Locate platelets.
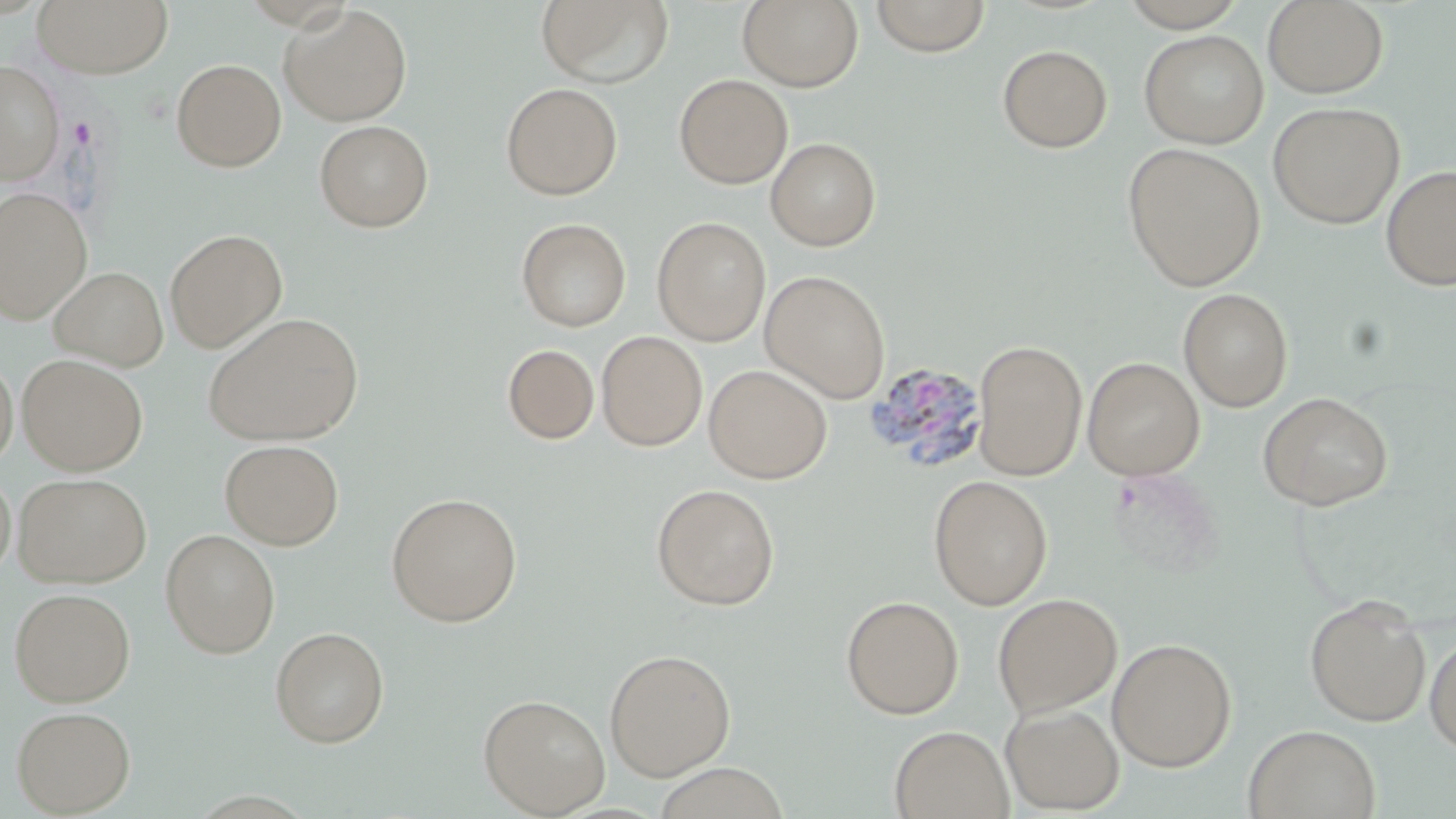
Approximate bounding boxes as (x1, y1, x2, y2) in pixels.
Platelets: (69, 118, 96, 147).

slide-level diagnosis = Plasmodium vivax
magnification = 1000x
image size = 1456×819 pixels
uninfected red blood cell locations = approximate bounding boxes as (x1, y1, x2, y2) in pixels: (33, 0, 174, 79), (535, 0, 674, 87), (738, 0, 864, 91), (869, 0, 991, 57), (1118, 0, 1249, 31), (1263, 0, 1389, 98), (279, 5, 412, 126), (1139, 29, 1268, 149), (997, 44, 1112, 153), (171, 58, 286, 172), (0, 61, 65, 184), (674, 73, 793, 189), (501, 82, 623, 200), (1267, 101, 1405, 229), (314, 120, 434, 232), (765, 136, 881, 251), (1122, 143, 1267, 290), (1381, 164, 1456, 291), (1, 187, 92, 322), (652, 216, 770, 345), (516, 217, 631, 331), (165, 229, 288, 352), (48, 265, 168, 371), (760, 269, 890, 402), (1178, 287, 1293, 412), (202, 312, 364, 446), (597, 331, 707, 451), (973, 340, 1087, 481), (502, 343, 599, 445), (19, 354, 148, 474), (0, 355, 17, 471), (1083, 357, 1204, 480), (703, 364, 832, 483), (1257, 391, 1393, 510), (219, 439, 345, 549), (0, 468, 16, 582), (14, 473, 152, 588), (928, 474, 1053, 610), (651, 482, 780, 610), (385, 492, 523, 626), (160, 528, 280, 657), (9, 587, 135, 706), (992, 592, 1122, 718), (1304, 594, 1432, 727), (841, 595, 964, 719), (270, 626, 389, 748), (1425, 631, 1456, 758), (1107, 637, 1237, 772), (604, 648, 736, 780), (478, 693, 610, 817), (1000, 703, 1124, 814), (11, 705, 136, 816), (1243, 724, 1381, 819), (890, 725, 1013, 819)
field of view = one of a larger specimen
modality = optical microscopy
stain = May-Grünwald-Giemsa
preparation = thin blood smear
Plasmodium vivax-infected red blood cell locations = approximate bounding boxes as (x1, y1, x2, y2) in pixels: (863, 360, 989, 475)